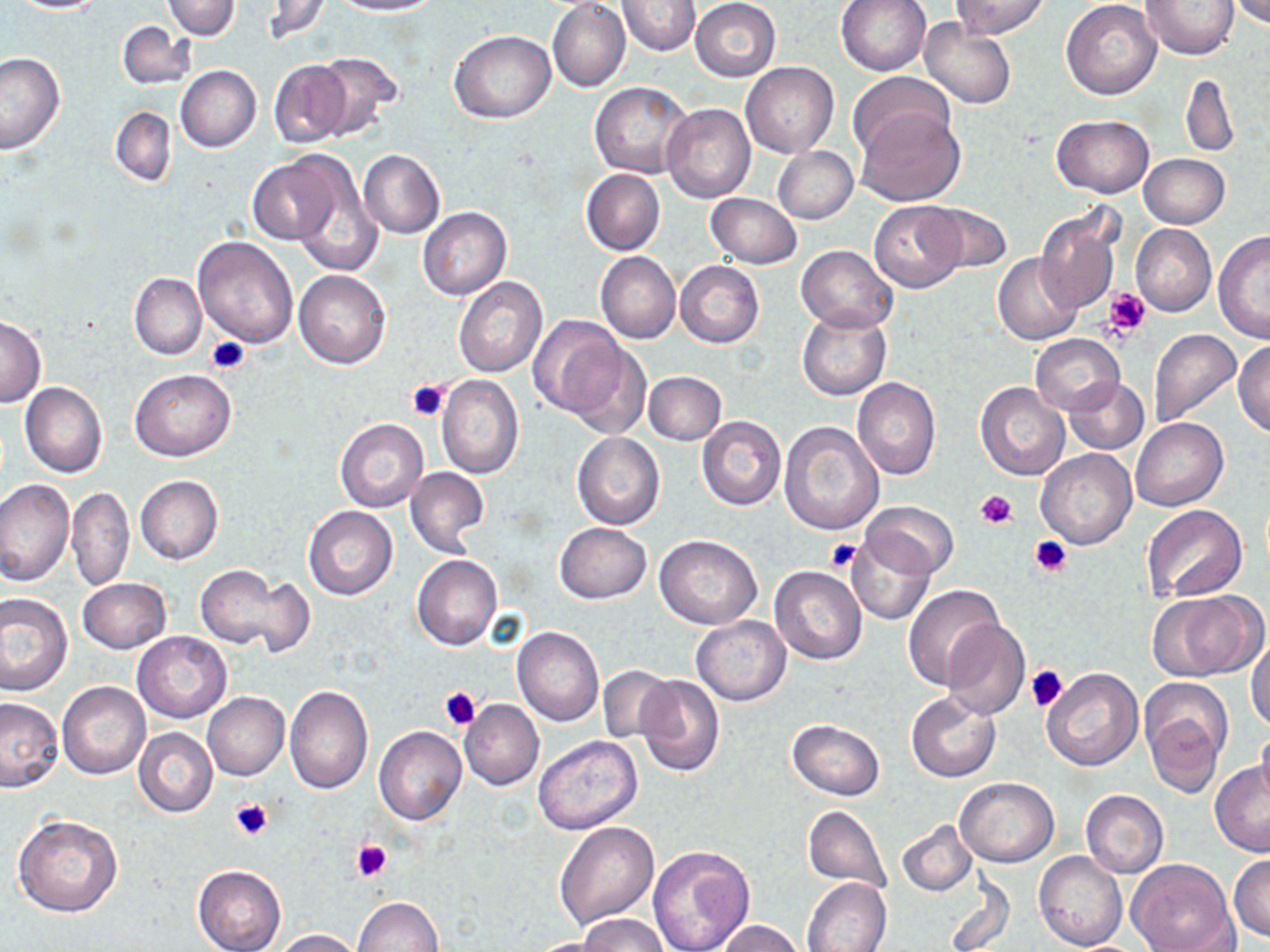
slide-level diagnosis = no evidence of blood parasites
modality = light microscopy
magnification = 1000x
stain = May-Grünwald-Giemsa
uninfected red blood cell locations = approximate bounding boxes as [x1, y1, x2, y2] in pixels: [11, 0, 107, 13], [161, 0, 240, 40], [259, 0, 330, 43], [332, 0, 442, 15], [835, 0, 931, 76], [952, 0, 1051, 39], [1061, 0, 1160, 100], [1140, 0, 1239, 60], [1231, 0, 1270, 27], [617, 1, 701, 55], [691, 1, 781, 81], [547, 2, 630, 93], [919, 18, 1017, 108], [118, 21, 196, 90], [449, 30, 556, 122], [0, 52, 66, 154], [311, 52, 403, 139], [268, 60, 352, 149], [741, 61, 838, 158], [176, 65, 261, 152], [848, 71, 953, 157], [1181, 73, 1239, 157], [590, 82, 695, 179], [662, 103, 755, 202], [855, 106, 966, 207], [110, 107, 177, 186], [1052, 114, 1153, 197], [772, 146, 858, 224], [359, 149, 445, 240], [1139, 154, 1230, 229], [249, 156, 341, 245], [290, 157, 383, 279], [581, 170, 665, 255], [707, 193, 802, 269], [695, 195, 788, 330], [868, 201, 967, 293], [924, 202, 1011, 275], [1037, 206, 1122, 314], [418, 207, 511, 300], [1131, 224, 1216, 316], [1213, 232, 1270, 344], [194, 234, 299, 349], [796, 245, 898, 333], [596, 252, 680, 343], [993, 252, 1083, 345], [676, 261, 764, 348], [295, 270, 391, 370], [130, 273, 206, 359], [453, 276, 548, 378], [796, 307, 892, 401], [529, 316, 628, 418], [0, 317, 46, 405], [1148, 329, 1242, 428], [1029, 334, 1125, 414], [1234, 341, 1270, 438], [565, 342, 651, 440], [131, 369, 236, 460], [645, 372, 727, 445], [437, 376, 524, 478], [1063, 377, 1149, 455], [852, 378, 940, 480], [20, 383, 107, 477], [975, 384, 1070, 482], [697, 417, 787, 510], [335, 418, 428, 512], [1132, 418, 1226, 511], [780, 421, 885, 537], [571, 431, 665, 530], [1036, 449, 1136, 550], [405, 466, 489, 556], [135, 475, 223, 565], [1, 479, 73, 586], [67, 485, 134, 591], [861, 501, 958, 579], [304, 505, 397, 600], [1146, 505, 1247, 602], [554, 523, 652, 603], [848, 534, 935, 625], [653, 535, 762, 629], [411, 554, 502, 650], [196, 563, 305, 653], [769, 565, 868, 665], [78, 577, 170, 654], [901, 584, 1006, 691], [1153, 591, 1266, 682], [0, 593, 73, 696], [690, 616, 790, 706], [942, 618, 1030, 719], [512, 626, 605, 726], [133, 630, 231, 723], [1247, 634, 1270, 732], [599, 665, 674, 742], [1040, 668, 1142, 771], [634, 676, 725, 776], [1139, 677, 1231, 792], [57, 682, 150, 781], [284, 684, 373, 795], [203, 692, 289, 780], [907, 692, 1001, 781], [0, 697, 64, 792], [460, 699, 544, 790], [787, 719, 885, 800], [134, 726, 217, 818], [374, 726, 466, 825], [1255, 726, 1270, 804], [534, 735, 643, 835], [1209, 761, 1270, 855], [956, 776, 1059, 866], [1079, 790, 1168, 878], [801, 804, 893, 895], [13, 814, 124, 918], [897, 819, 977, 895], [554, 820, 659, 930], [648, 844, 755, 952], [1035, 851, 1128, 951], [1228, 852, 1270, 941], [1125, 858, 1237, 952], [192, 865, 286, 952], [944, 873, 1016, 952], [802, 876, 891, 952], [352, 897, 445, 952], [577, 914, 669, 951], [718, 919, 805, 952], [275, 929, 363, 951], [520, 937, 620, 952]
image size = 1270×952 pixels
platelet locations = approximate bounding boxes as [x1, y1, x2, y2] in pixels: [1104, 288, 1152, 335], [206, 334, 251, 375], [407, 379, 449, 422], [974, 489, 1018, 531], [1028, 536, 1072, 579], [826, 539, 861, 573], [1024, 664, 1068, 711], [439, 687, 480, 730], [230, 799, 274, 841], [351, 838, 392, 883]
field of view = one of a larger specimen
preparation = thin blood smear